Identify the parasite.
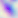
Toxoplasma gondii.

Photomicrograph. 400x magnification.